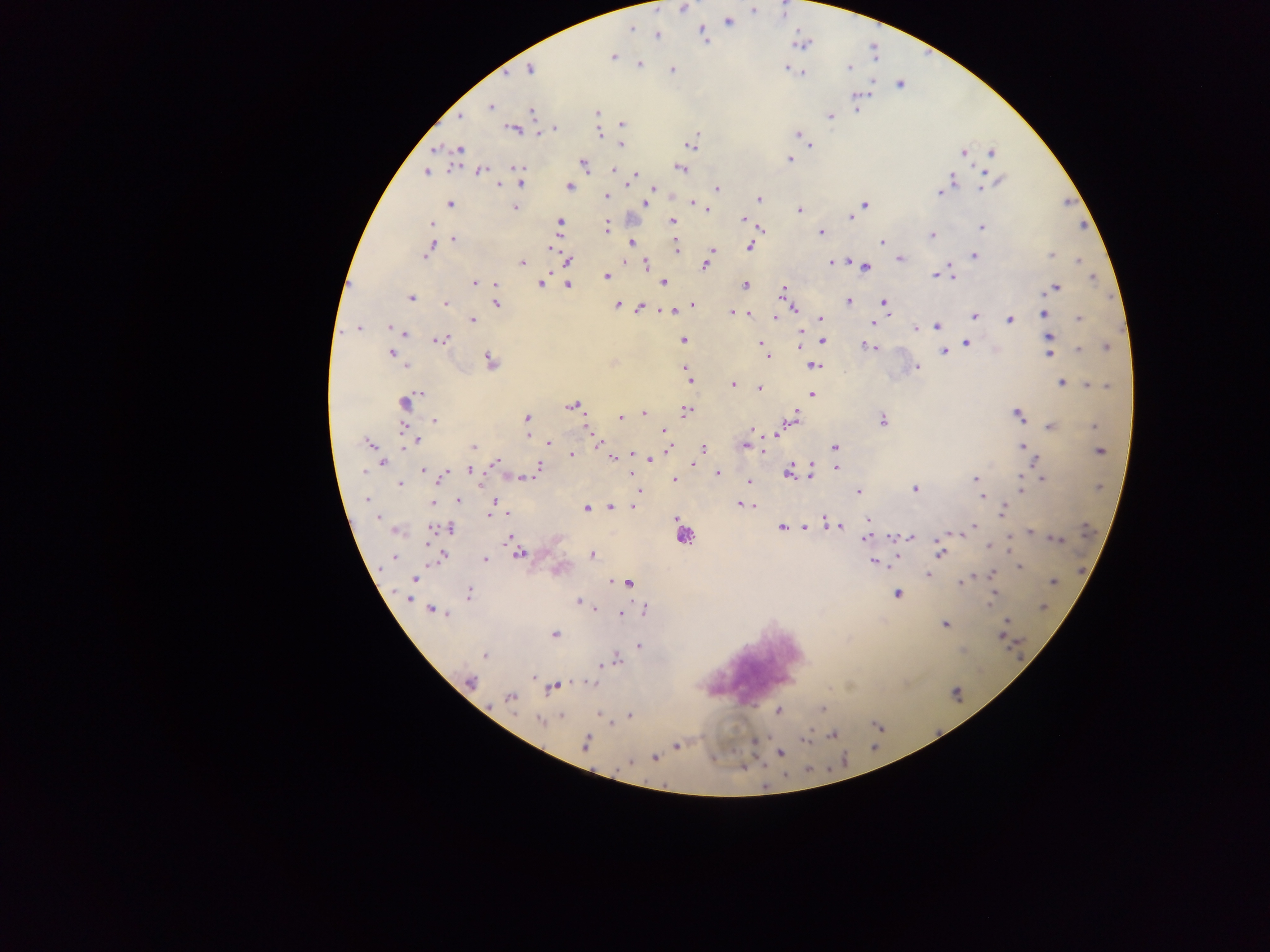
{
  "field_of_view": "single",
  "preparation": "thick blood smear",
  "capture": "mobile-phone photograph through a microscope",
  "image_size": "1270×952 pixels",
  "leukocyte_locations": "approximate centers as x y in pixels: 680 539",
  "country": "Ghana",
  "malaria_parasite_locations": "approximate centers as x y in pixels: 684 8; 752 10; 729 21; 630 28; 702 30; 613 57; 639 63; 787 68; 529 69; 671 69; 848 69; 803 74; 490 106; 531 112; 596 113; 829 116; 461 117; 621 123; 512 129; 798 132; 600 135; 621 145; 811 145; 436 149; 461 149; 991 153; 963 155; 789 159; 584 166; 521 168; 449 169; 680 169; 479 170; 615 171; 426 172; 985 172; 636 173; 950 176; 955 179; 1002 180; 520 186; 569 186; 629 186; 497 187; 653 187; 980 187; 717 188; 941 194; 606 196; 758 198; 645 202; 692 202; 450 203; 865 204; 515 208; 708 209; 798 211; 850 217; 742 219; 671 220; 746 221; 558 222; 433 224; 606 224; 981 228; 760 230; 820 233; 931 235; 455 240; 630 243; 881 243; 676 246; 431 247; 751 248; 552 249; 712 250; 427 252; 425 256; 1051 256; 973 257; 899 258; 846 259; 569 262; 520 265; 646 265; 829 265; 705 266; 866 267; 610 274; 952 275; 933 276; 606 277; 1091 280; 472 282; 662 282; 480 283; 542 283; 568 284; 494 285; 744 285; 1057 287; 783 291; 410 297; 849 300; 884 302; 445 305; 496 306; 616 306; 694 306; 640 308; 886 308; 793 310; 671 313; 731 313; 751 314; 1044 315; 973 316; 774 318; 1079 319; 822 320; 472 321; 1009 321; 872 323; 359 328; 390 328; 935 328; 915 329; 800 330; 407 334; 1052 336; 684 339; 825 340; 443 341; 759 341; 967 343; 868 345; 872 346; 799 347; 1079 349; 943 352; 391 354; 1049 354; 489 358; 768 358; 814 366; 409 369; 917 369; 689 381; 1060 382; 1087 384; 734 386; 759 389; 421 392; 811 394; 410 399; 406 403; 572 407; 645 412; 686 412; 797 412; 1019 414; 527 417; 623 418; 433 421; 1050 426; 1093 426; 401 427; 659 429; 587 430; 751 430; 777 431; 663 432; 527 434; 599 440; 417 442; 549 444; 369 445; 1023 446; 745 447; 472 448; 703 448; 752 448; 834 449; 669 450; 765 451; 1101 451; 573 455; 611 456; 651 460; 495 462; 383 464; 813 464; 694 465; 836 467; 539 468; 814 469; 360 471; 423 471; 470 471; 425 472; 718 472; 788 473; 812 473; 1022 473; 364 474; 476 475; 442 478; 519 478; 530 478; 975 479; 673 480; 1043 480; 748 481; 399 484; 913 487; 1021 488; 639 489; 859 492; 981 497; 368 500; 460 500; 494 502; 740 503; 431 504; 610 504; 631 505; 747 506; 586 509; 1004 509; 508 513; 489 516; 869 519; 377 520; 825 520; 434 527; 782 527; 804 528; 969 528; 447 529; 1032 531; 429 532; 962 534; 865 538; 911 538; 1054 538; 507 539; 890 539; 425 545; 987 546; 1012 546; 940 553; 520 554; 592 554; 485 560; 873 563; 1020 567; 991 573; 927 576; 416 580; 961 582; 612 583; 628 583; 1051 583; 995 593; 471 594; 897 595; 991 597; 408 600; 577 600; 991 606; 431 609; 595 609; 449 615; 620 615; 1005 621; 945 625; 555 635; 640 645; 484 655; 618 660; 599 665; 592 682; 469 683; 556 687; 509 698; 821 707; 779 712; 598 713; 631 716; 561 717; 539 722; 806 737; 803 741; 585 744; 677 747; 781 753; 655 758; 628 763"
}